Assess for malaria.
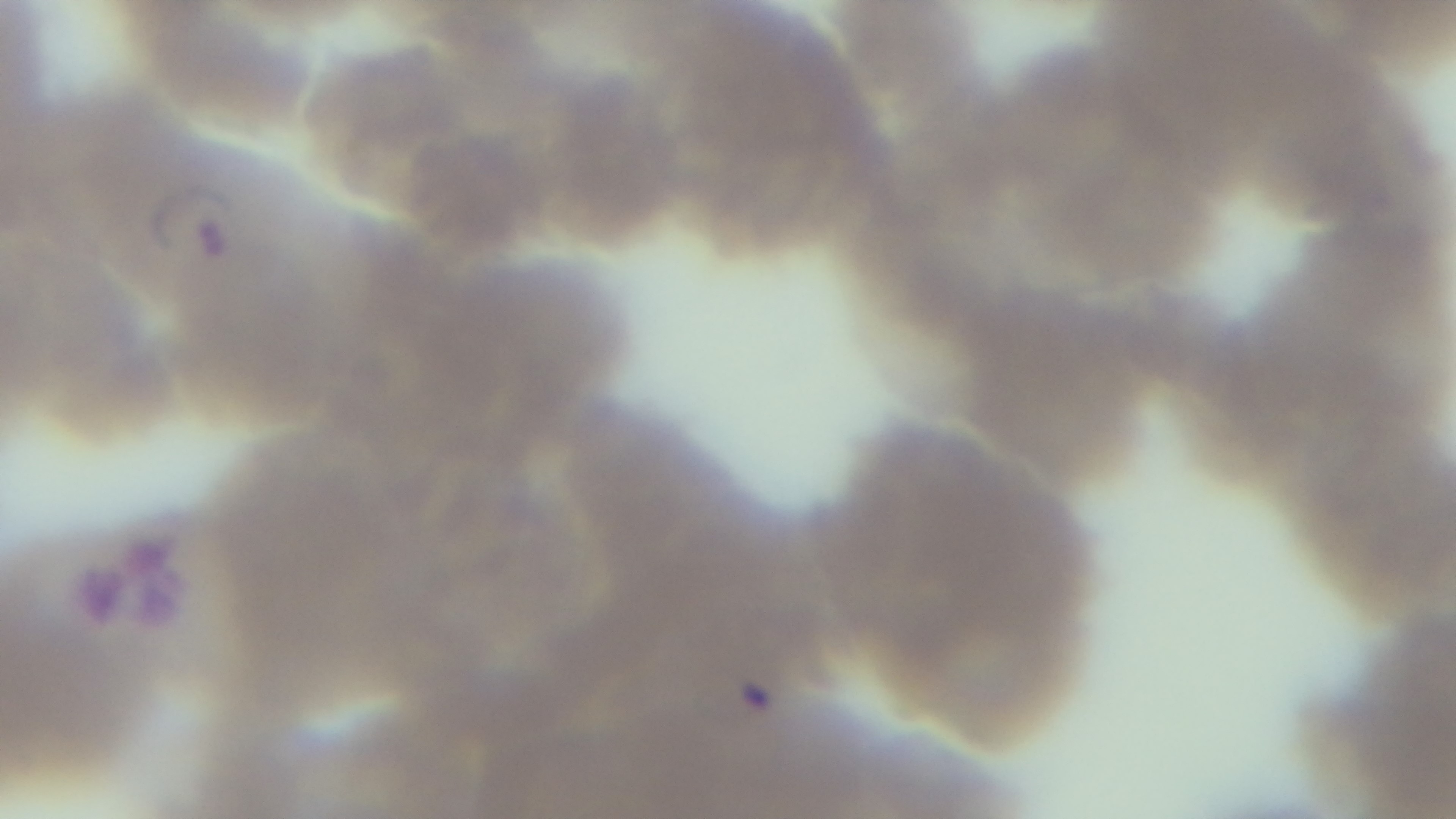

It is infected.

field_of_view: one from the slide
objective: 100x oil immersion
stain: Giemsa
modality: light microscopy
preparation: thin
capture: mounted 4K digital camera